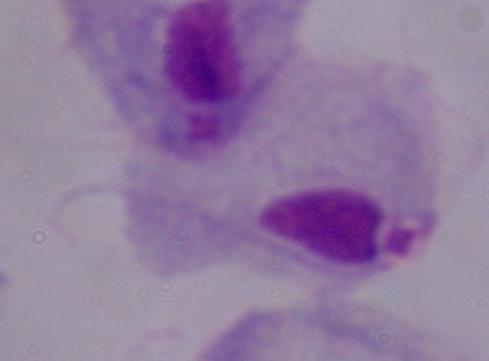
Summary:
  - Modality: micrograph
  - Magnification: 1000x
  - Identification: trichomonad